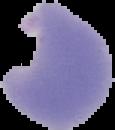
Image is 115×130 pixels. From a thin blood smear. The area outside the segmented cell region is set to black. Result: Plasmodium parasites identified.